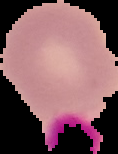

Summary:
  - Image type: segmented cell region with the area outside set to black
  - Result: negative for Plasmodium parasites
  - Preparation: thin blood smear
  - Image size: 118×154 pixels